Outline each Plasmodium falciparum-infected red blood cell.
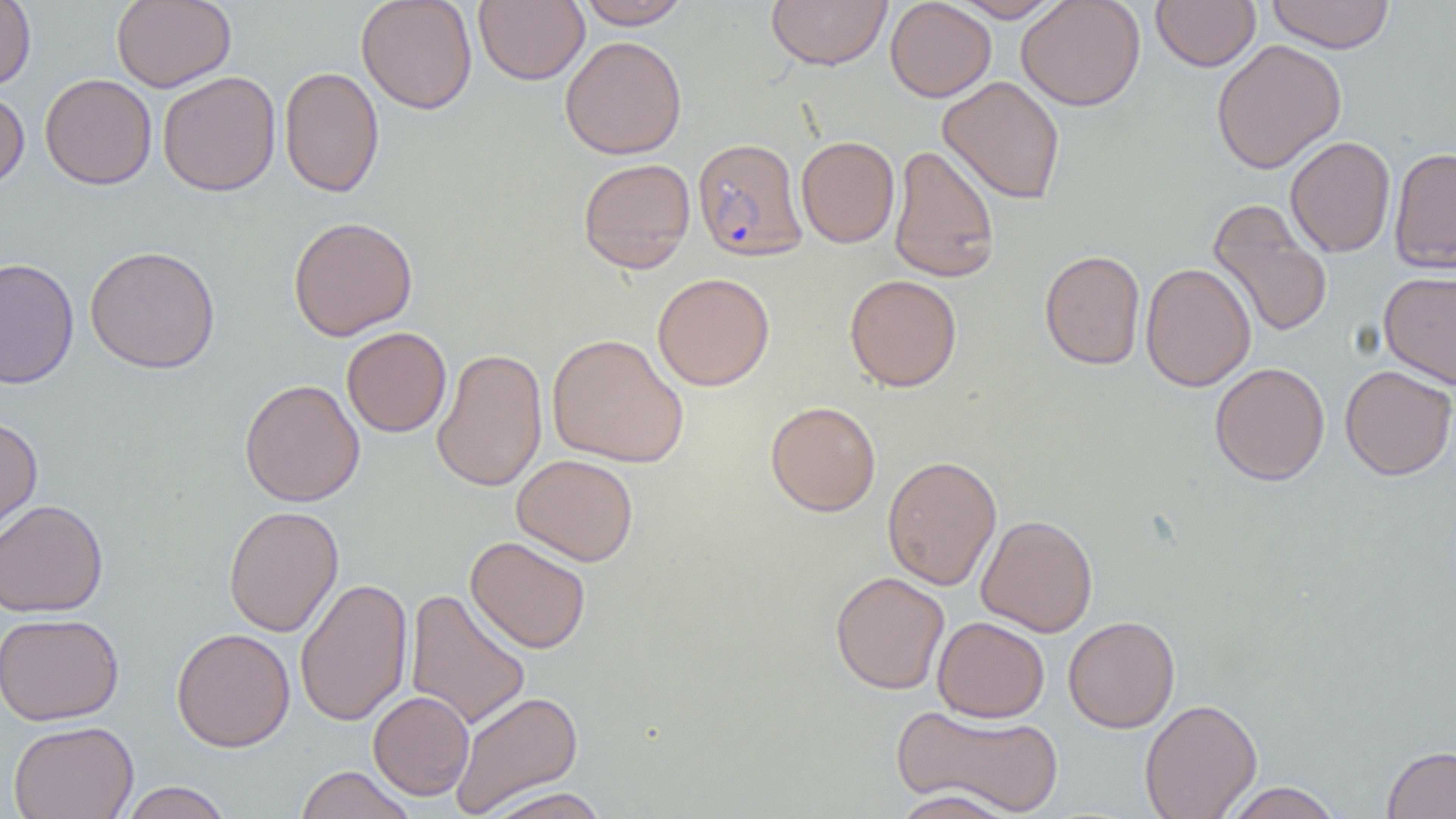

Approximate bounding boxes as (x1, y1, x2, y2) in pixels.
Plasmodium falciparum-infected red blood cells: (692, 137, 808, 263).

slide-level diagnosis = Plasmodium falciparum
image size = 1456×819 pixels
preparation = thin blood smear
uninfected red blood cell locations = approximate bounding boxes as (x1, y1, x2, y2) in pixels: (0, 0, 36, 90), (112, 0, 236, 91), (356, 0, 477, 114), (473, 0, 589, 85), (766, 0, 892, 70), (885, 0, 996, 102), (949, 0, 1065, 22), (1016, 0, 1146, 111), (1151, 0, 1261, 72), (1265, 0, 1395, 53), (576, 1, 692, 30), (560, 35, 687, 160), (1211, 39, 1347, 174), (279, 66, 385, 198), (157, 71, 281, 196), (40, 73, 157, 190), (937, 75, 1065, 205), (0, 87, 29, 194), (796, 136, 900, 248), (1284, 136, 1396, 257), (888, 144, 1000, 283), (1388, 146, 1456, 272), (577, 157, 696, 274), (1207, 199, 1333, 339), (288, 216, 418, 341), (84, 245, 221, 374), (1039, 249, 1146, 370), (0, 256, 79, 390), (1140, 262, 1256, 392), (1378, 270, 1456, 389), (652, 272, 775, 391), (845, 274, 962, 392), (341, 327, 451, 437), (546, 333, 689, 468), (431, 347, 548, 493), (1210, 362, 1330, 486), (1339, 364, 1456, 481), (239, 379, 365, 506), (765, 400, 881, 517), (0, 415, 43, 542), (511, 454, 638, 566), (882, 455, 1002, 590), (0, 498, 109, 618), (223, 505, 344, 637), (976, 514, 1098, 637), (465, 535, 591, 654), (830, 571, 949, 695), (295, 577, 413, 726), (404, 588, 531, 731), (0, 612, 125, 725), (1063, 615, 1180, 733), (933, 616, 1049, 723), (171, 627, 295, 752), (450, 690, 584, 817), (368, 691, 475, 800), (1140, 698, 1262, 819), (891, 704, 1064, 816), (7, 720, 138, 819), (1382, 745, 1456, 819), (293, 765, 416, 819), (118, 782, 234, 819), (1221, 782, 1343, 819), (482, 786, 611, 819), (888, 789, 1021, 819)
magnification = 1000x
modality = light microscopy
field of view = single